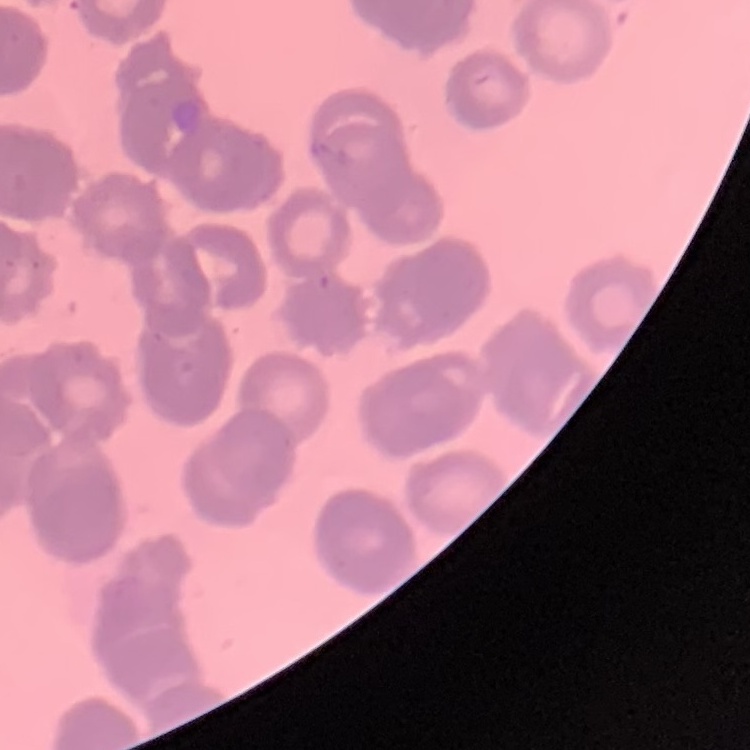
Summary:
  - Erythrocyte morphology: rouleaux formation
  - Image type: square crop of a larger photomicrograph
  - Stain: Field's or Giemsa
  - Preparation: thin blood film